Give the position of every Plasmodium parasite visible.
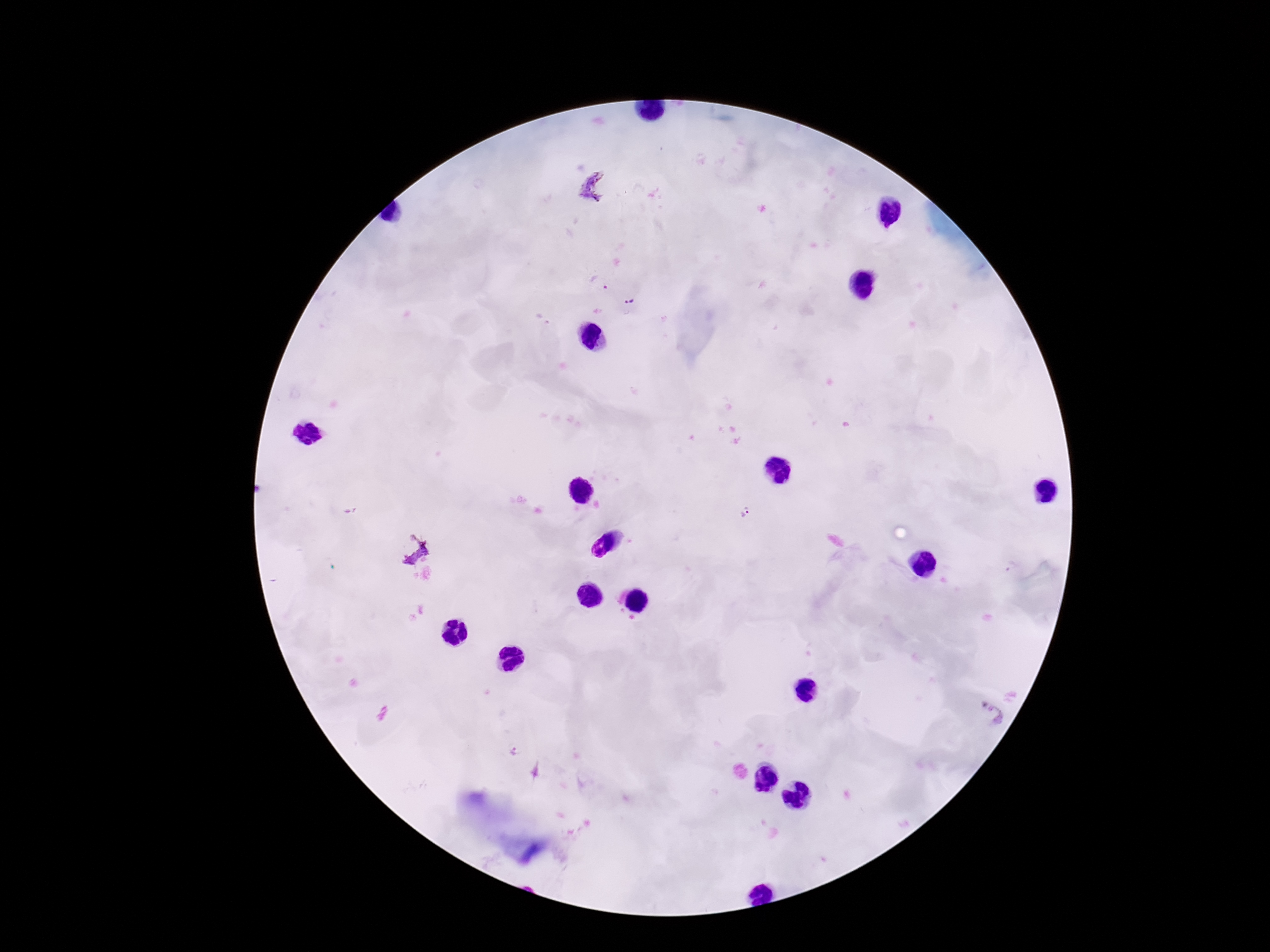
Approximate object centers, in pixels from the top-left corner.
Plasmodium parasites: (x=592, y=187), (x=598, y=281), (x=628, y=300), (x=745, y=512), (x=409, y=546), (x=997, y=714), (x=512, y=753).

Thick blood smear. Patient malaria status: positive. 100x magnification. Giemsa-stained preparation. Image is 1270×952 pixels. Smartphone photograph taken through the microscope eyepiece. One field from this slide.